Assess this cell for malaria.
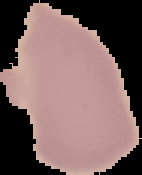

It is uninfected.

image_type: cell region segmented out of the field of view; surrounding area masked to black
preparation: thin blood film
image_size: 142×175 pixels